Locate every blood parasite and identify its species.
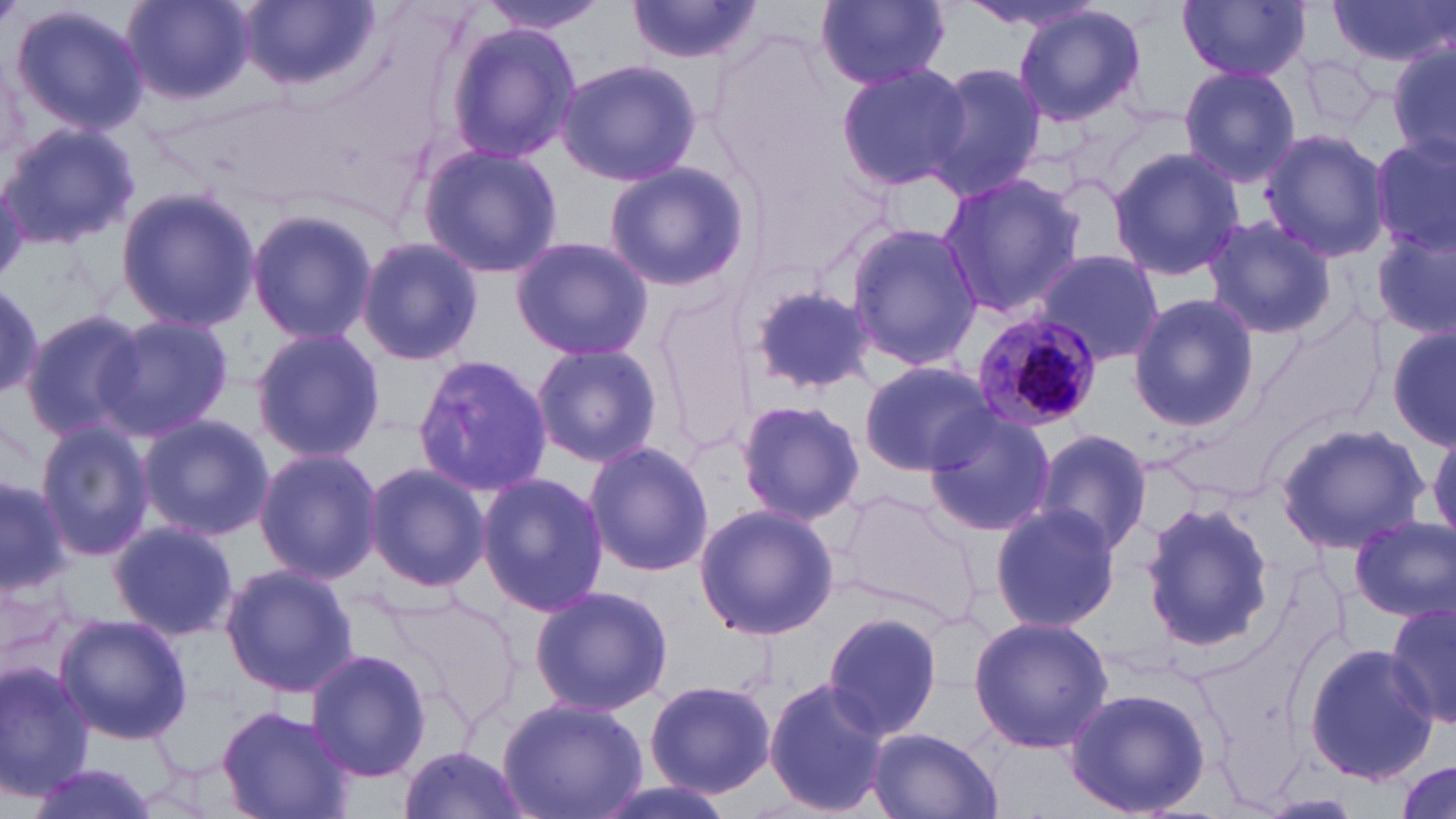

Approximate bounding boxes as named x1/y1/x2/y2 corners in pixels.
Plasmodium malariae-infected red blood cells: (x1=971, y1=311, x2=1101, y2=431).
No Plasmodium falciparum, Plasmodium ovale, Plasmodium vivax, Babesia divergens, or Trypanosoma brucei observed.

Uninfected red blood cell locations: (x1=120, y1=0, x2=256, y2=106), (x1=814, y1=0, x2=950, y2=90), (x1=955, y1=0, x2=1115, y2=37), (x1=1178, y1=0, x2=1310, y2=82), (x1=1326, y1=0, x2=1454, y2=70), (x1=478, y1=1, x2=608, y2=34), (x1=239, y1=2, x2=378, y2=94), (x1=624, y1=2, x2=768, y2=65), (x1=9, y1=3, x2=150, y2=138), (x1=1012, y1=6, x2=1146, y2=127), (x1=445, y1=22, x2=582, y2=166), (x1=1388, y1=43, x2=1456, y2=168), (x1=1300, y1=51, x2=1383, y2=133), (x1=555, y1=58, x2=701, y2=187), (x1=922, y1=61, x2=1045, y2=197), (x1=835, y1=62, x2=969, y2=192), (x1=1178, y1=64, x2=1304, y2=188), (x1=1, y1=123, x2=139, y2=248), (x1=1260, y1=130, x2=1392, y2=261), (x1=1371, y1=138, x2=1456, y2=259), (x1=419, y1=143, x2=562, y2=279), (x1=1107, y1=147, x2=1245, y2=282), (x1=604, y1=161, x2=749, y2=292), (x1=937, y1=172, x2=1084, y2=318), (x1=115, y1=188, x2=263, y2=330), (x1=245, y1=207, x2=376, y2=348), (x1=1202, y1=214, x2=1337, y2=340), (x1=844, y1=224, x2=985, y2=368), (x1=1373, y1=227, x2=1455, y2=342), (x1=357, y1=236, x2=482, y2=366), (x1=509, y1=236, x2=655, y2=362), (x1=1031, y1=249, x2=1165, y2=367), (x1=742, y1=280, x2=882, y2=395), (x1=0, y1=284, x2=45, y2=397), (x1=1127, y1=293, x2=1260, y2=431), (x1=1251, y1=307, x2=1387, y2=447), (x1=20, y1=308, x2=148, y2=441), (x1=99, y1=312, x2=232, y2=441), (x1=1388, y1=322, x2=1455, y2=449), (x1=249, y1=327, x2=385, y2=464), (x1=530, y1=343, x2=663, y2=467), (x1=413, y1=354, x2=553, y2=498), (x1=858, y1=359, x2=998, y2=475), (x1=736, y1=398, x2=865, y2=525), (x1=921, y1=409, x2=1058, y2=536), (x1=138, y1=415, x2=272, y2=539), (x1=1275, y1=421, x2=1431, y2=553), (x1=34, y1=423, x2=155, y2=562), (x1=1430, y1=424, x2=1456, y2=545), (x1=1032, y1=429, x2=1155, y2=558), (x1=582, y1=441, x2=714, y2=577), (x1=252, y1=447, x2=382, y2=582), (x1=364, y1=462, x2=488, y2=593), (x1=476, y1=470, x2=609, y2=615), (x1=0, y1=479, x2=72, y2=597), (x1=834, y1=490, x2=985, y2=626), (x1=1138, y1=501, x2=1276, y2=654), (x1=693, y1=502, x2=840, y2=642), (x1=988, y1=503, x2=1122, y2=634), (x1=1349, y1=516, x2=1455, y2=622), (x1=108, y1=520, x2=237, y2=641), (x1=218, y1=563, x2=360, y2=699), (x1=529, y1=584, x2=672, y2=718), (x1=381, y1=590, x2=519, y2=718), (x1=1385, y1=601, x2=1456, y2=733), (x1=822, y1=612, x2=944, y2=741), (x1=56, y1=614, x2=190, y2=745), (x1=968, y1=615, x2=1114, y2=755), (x1=1303, y1=642, x2=1439, y2=786), (x1=304, y1=647, x2=433, y2=782), (x1=0, y1=660, x2=99, y2=799), (x1=223, y1=673, x2=426, y2=804), (x1=645, y1=677, x2=777, y2=798), (x1=762, y1=677, x2=888, y2=818), (x1=1062, y1=686, x2=1212, y2=818), (x1=498, y1=697, x2=647, y2=819), (x1=218, y1=705, x2=355, y2=818), (x1=865, y1=726, x2=1004, y2=819), (x1=396, y1=744, x2=531, y2=819), (x1=22, y1=761, x2=165, y2=819), (x1=1393, y1=761, x2=1453, y2=817), (x1=585, y1=777, x2=742, y2=819), (x1=1255, y1=795, x2=1364, y2=817). Slide-level diagnosis: Plasmodium malariae. Captured at 1000x magnification. May-Grünwald-Giemsa stain. Thin blood smear. Single field of view. Optical microscopy. Image is 1456×819 pixels.